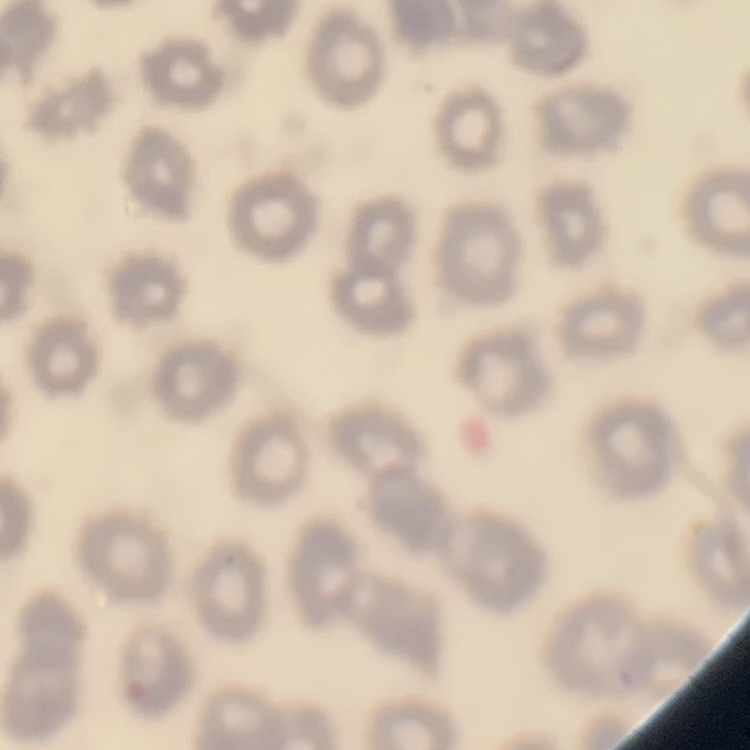
erythrocyte_morphology: no rouleaux formation
stain: Field's or Giemsa
image_type: square crop of a larger photomicrograph
preparation: thin blood film